Give the position of every Plasmodium parasite.
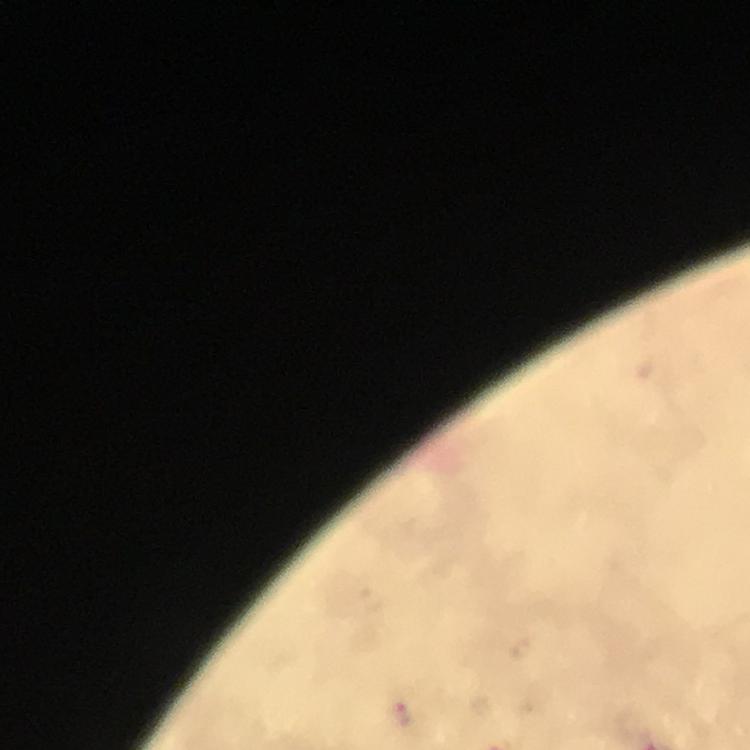
Approximate object centers, in pixels from the top-left corner.
Plasmodium parasites: (x=403, y=714).

Image is 750×750 pixels. Immersion oil was used. From a diagnostic examination for malaria. 100x magnification. Thick smear. Photographed with a smartphone mounted on the microscope. Giemsa stain. A crop from one field of view.